Assess the morphology of the red blood cells.
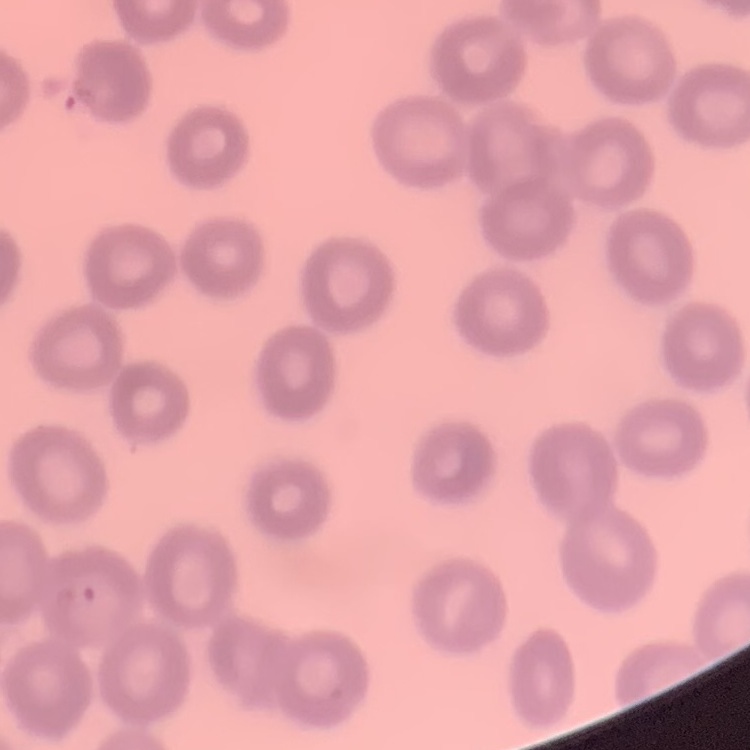

No rouleaux formation.

Summary:
  - Stain: Field's or Giemsa
  - Image type: one tile cut from a larger photomicrograph
  - Preparation: thin blood smear